Classify this cell by malaria status.
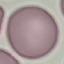

Uninfected.

stain = Giemsa
capture = smartphone camera at the microscope eyepiece
preparation = thin blood film
image type = automatically extracted cell patch, resized to 64 × 64 pixels